State the blood parasite species.
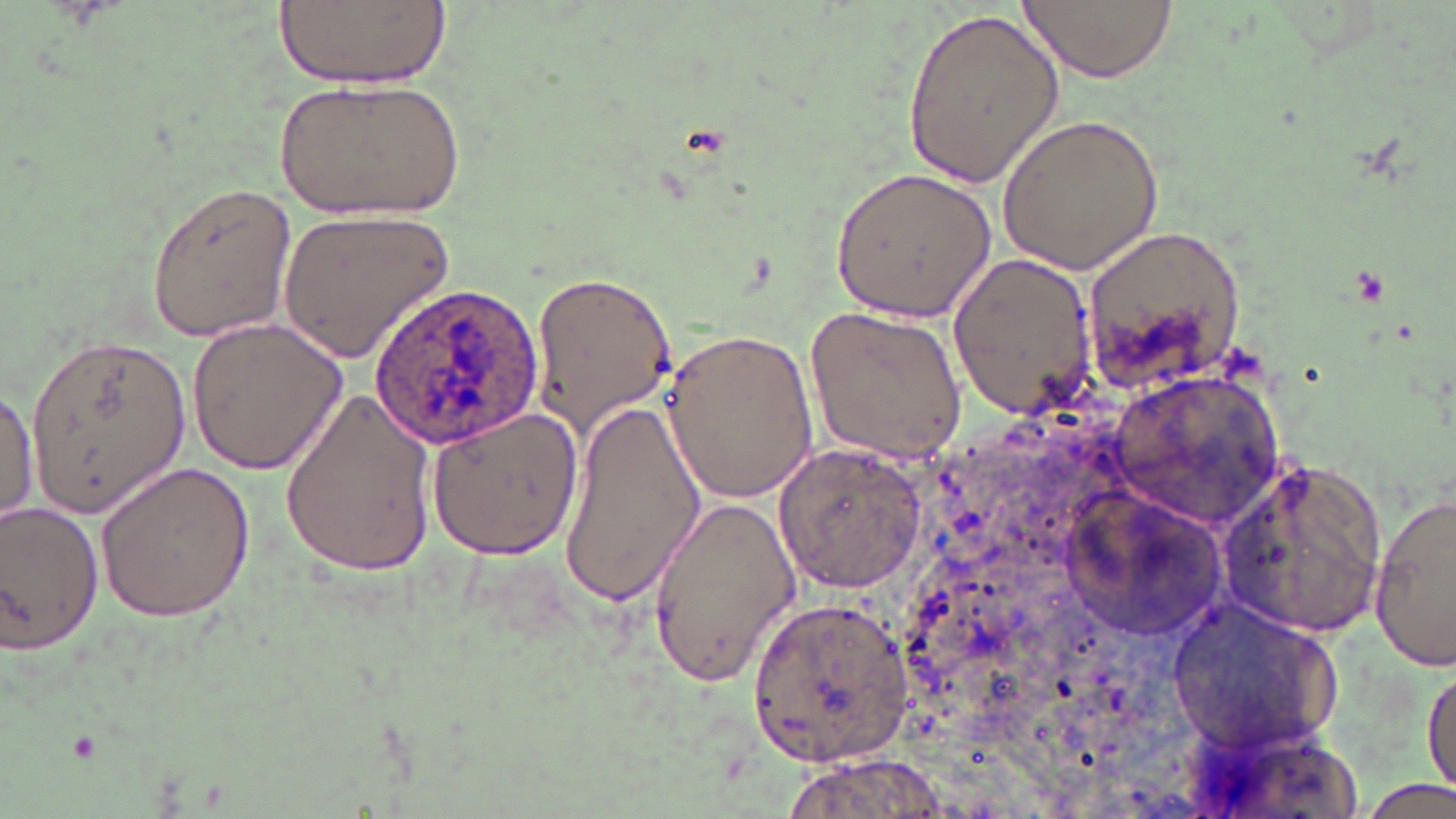
Plasmodium ovale.

image size = 1456×819 pixels
uninfected red blood cell locations = approximate bounding boxes as (x1, y1, x2, y2) in pixels: (276, 0, 448, 86), (1017, 0, 1179, 83), (900, 5, 1064, 191), (278, 76, 463, 221), (997, 112, 1166, 274), (828, 166, 999, 323), (145, 179, 299, 344), (276, 210, 452, 367), (949, 253, 1098, 414), (529, 269, 678, 437), (805, 306, 968, 460), (186, 317, 347, 476), (659, 326, 819, 505), (27, 336, 192, 519), (280, 384, 439, 580), (0, 385, 38, 528), (555, 396, 704, 607), (423, 404, 583, 558), (773, 443, 929, 595), (1221, 458, 1388, 636), (96, 461, 257, 622), (1368, 492, 1455, 671), (648, 493, 803, 687), (0, 500, 105, 656), (747, 592, 915, 770), (1165, 597, 1341, 757), (1422, 658, 1455, 800), (1362, 778, 1455, 818)
field of view = single
magnification = 1000x
stain = May-Grünwald-Giemsa
modality = optical microscopy
Plasmodium ovale-infected red blood cell locations = approximate bounding boxes as (x1, y1, x2, y2) in pixels: (367, 282, 542, 449)
preparation = thin blood smear